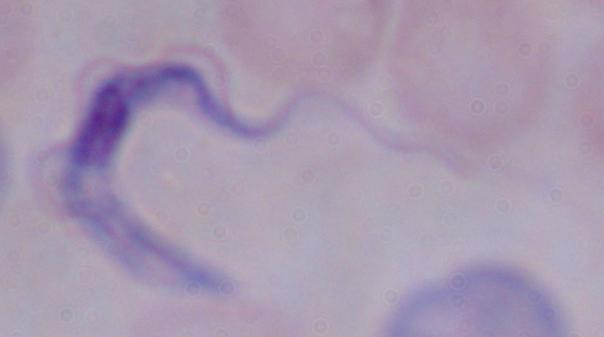
Summary:
  - Identification: trypanosome
  - Modality: micrograph
  - Magnification: 1000x